Locate every malaria parasite.
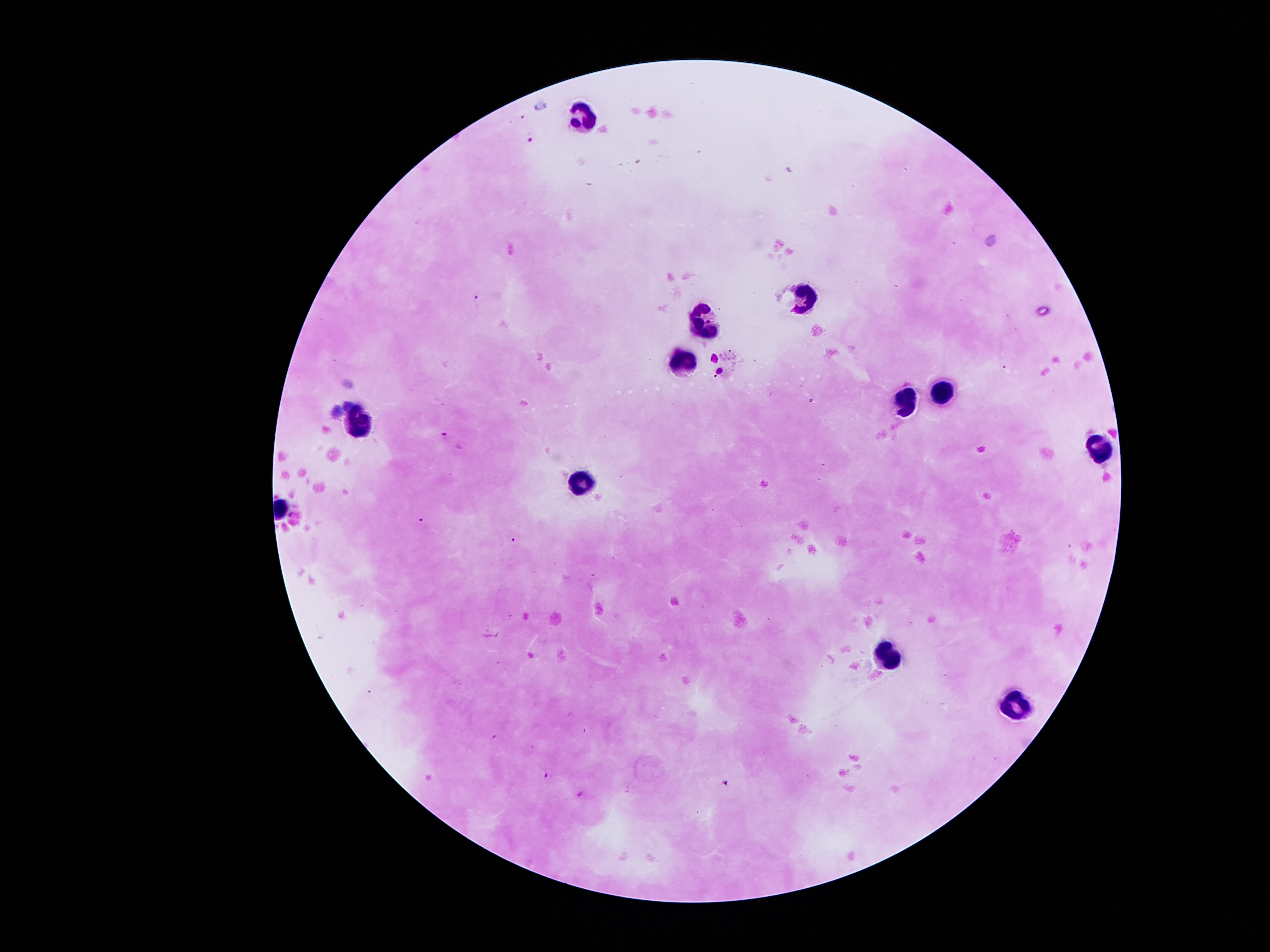

Approximate centers as {x, y} in pixels.
Malaria parasites: {532, 138}, {476, 297}, {444, 435}, {420, 520}, {513, 539}, {547, 775}, {725, 781}, {579, 794}.

Summary:
  - Leukocyte locations: {588, 114}, {807, 297}, {709, 320}, {679, 357}, {944, 389}, {902, 406}, {363, 418}, {1101, 449}, {583, 478}, {890, 651}, {1017, 702}
  - Magnification: 100x
  - Capture: smartphone through the microscope eyepiece
  - Image size: 1270×952 pixels
  - Patient malaria status: infected with Plasmodium falciparum
  - Field of view: one from this slide
  - Preparation: thick blood film
  - Stain: Giemsa